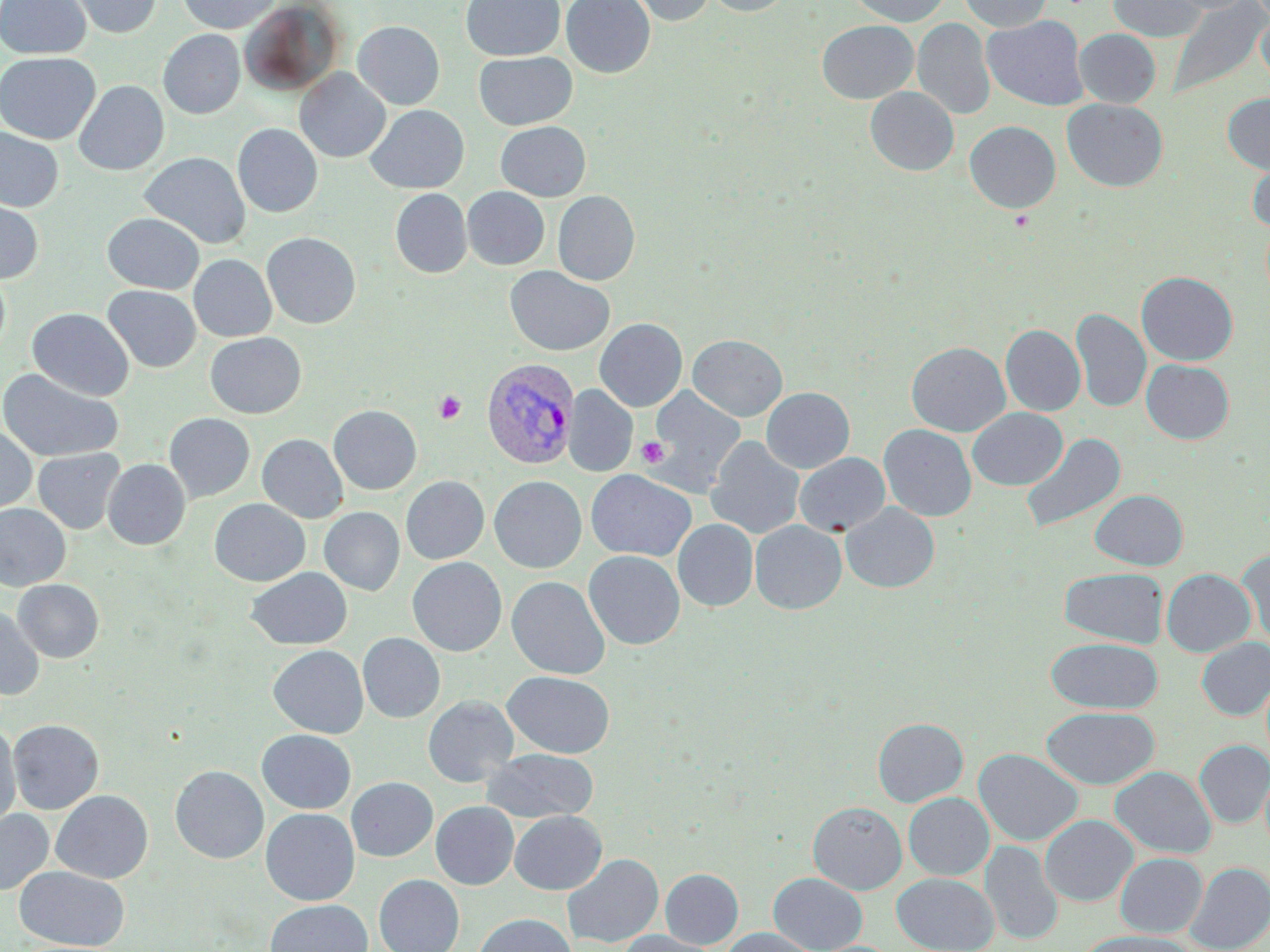
Approximate bounding boxes as [x1, y1, x2, y2] in pixels. Plasmodium vivax-infected red blood cell locations: [481, 358, 580, 469]. Platelet locations: [1009, 210, 1034, 231], [434, 391, 466, 424], [636, 436, 669, 468]. Uninfected red blood cell locations: [0, 0, 91, 58], [66, 0, 161, 38], [177, 0, 282, 34], [460, 0, 565, 61], [561, 0, 655, 78], [627, 0, 715, 26], [705, 0, 793, 16], [848, 0, 951, 27], [959, 0, 1052, 32], [1107, 0, 1207, 42], [1164, 0, 1255, 15], [1167, 1, 1268, 100], [238, 2, 345, 95], [1256, 12, 1270, 91], [982, 15, 1088, 111], [912, 18, 995, 120], [817, 20, 918, 104], [353, 21, 445, 109], [158, 29, 245, 119], [1074, 29, 1161, 108], [473, 51, 577, 130], [0, 52, 100, 144], [295, 68, 390, 162], [74, 80, 169, 175], [865, 87, 958, 176], [1222, 93, 1270, 174], [1062, 98, 1168, 192], [365, 104, 469, 193], [964, 120, 1061, 213], [495, 121, 591, 201], [232, 123, 323, 218], [0, 127, 64, 212], [139, 151, 251, 249], [1247, 157, 1270, 233], [462, 187, 549, 270], [390, 188, 472, 278], [553, 190, 640, 285], [0, 196, 45, 284], [102, 212, 205, 293], [261, 232, 361, 329], [188, 254, 277, 342], [504, 265, 615, 356], [0, 266, 10, 359], [1136, 272, 1238, 366], [102, 285, 201, 372], [27, 307, 134, 401], [1070, 308, 1151, 413], [594, 318, 687, 411], [1001, 324, 1085, 416], [205, 332, 306, 418], [687, 334, 788, 421], [906, 341, 1010, 437], [1141, 359, 1234, 444], [0, 367, 124, 463], [563, 385, 638, 476], [645, 386, 746, 497], [761, 387, 855, 473], [329, 405, 422, 494], [967, 408, 1067, 490], [164, 413, 255, 503], [0, 424, 37, 514], [879, 424, 977, 521], [1019, 432, 1126, 535], [257, 434, 348, 523], [705, 436, 805, 539], [32, 448, 125, 534], [794, 453, 890, 537], [103, 458, 190, 549], [585, 469, 697, 561], [401, 476, 489, 564], [489, 476, 587, 573], [1090, 489, 1188, 570], [210, 499, 310, 586], [841, 502, 940, 592], [0, 503, 71, 591], [6, 503, 83, 663], [319, 507, 405, 595], [673, 519, 758, 611], [750, 520, 846, 614], [1238, 547, 1269, 647], [584, 550, 685, 650], [407, 557, 507, 656], [246, 567, 352, 650], [1059, 567, 1168, 648], [1161, 568, 1256, 657], [507, 576, 610, 679], [13, 579, 104, 663], [0, 605, 44, 701], [358, 633, 445, 723], [1046, 637, 1163, 714], [1196, 637, 1270, 720], [268, 645, 368, 738], [503, 671, 614, 758], [423, 695, 518, 787], [1041, 707, 1159, 789], [873, 717, 968, 806], [7, 719, 104, 814], [0, 724, 21, 830], [256, 729, 356, 814], [1195, 741, 1270, 828], [481, 748, 598, 823], [974, 749, 1083, 846], [170, 765, 268, 863], [1110, 766, 1216, 859], [346, 777, 438, 861], [50, 790, 153, 883], [903, 793, 994, 880], [431, 802, 518, 889], [808, 802, 906, 894], [261, 808, 359, 905], [0, 809, 54, 895], [510, 810, 606, 894], [1040, 815, 1137, 906], [981, 840, 1063, 945], [1115, 853, 1207, 937], [563, 854, 664, 947], [1185, 862, 1270, 952], [15, 866, 129, 950], [660, 868, 743, 948], [769, 873, 866, 952], [892, 873, 997, 952], [374, 874, 464, 952], [265, 899, 372, 952], [473, 913, 577, 952], [722, 927, 816, 952], [618, 930, 715, 952], [1076, 932, 1197, 952]. Slide-level diagnosis: Plasmodium vivax. 1000x magnification. Thin blood film. Optical microscopy. Image is 1270×952 pixels. One field of a larger specimen. May-Grünwald-Giemsa-stained preparation.